Classify this cell by malaria status.
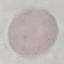

Uninfected.

Summary:
  - Stain: Giemsa
  - Preparation: thin blood smear
  - Image type: cell patch, automatically extracted from a larger field of view and resized to 64 × 64 pixels
  - Capture: smartphone through the microscope eyepiece